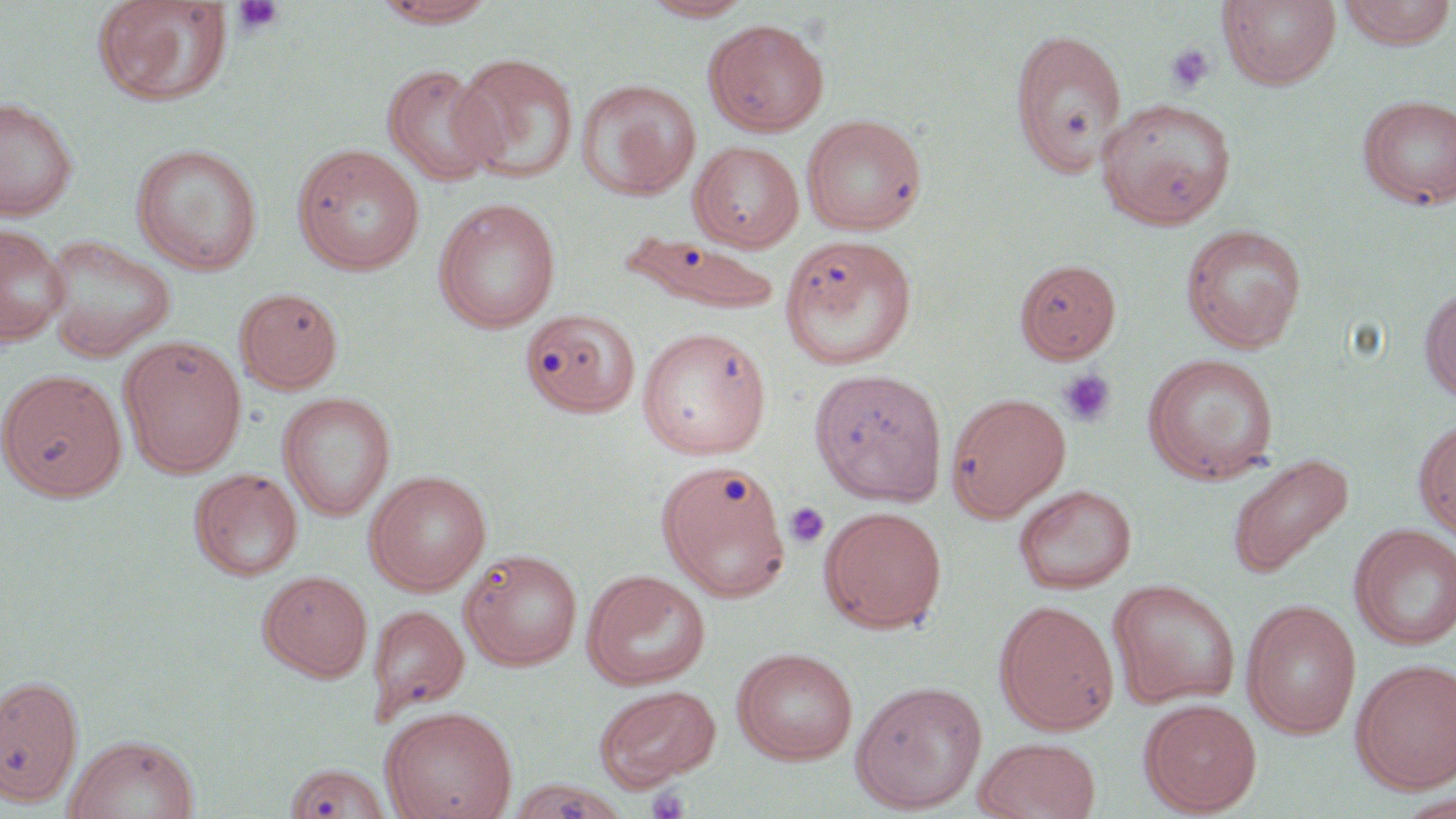
Approximate bounding boxes as named x1/y1/x2/y2 corners in pixels. Platelet locations: (x1=231, y1=0, x2=286, y2=36), (x1=1165, y1=43, x2=1215, y2=94), (x1=1058, y1=369, x2=1117, y2=427), (x1=784, y1=502, x2=830, y2=549), (x1=646, y1=787, x2=691, y2=819). Uninfected red blood cell locations: (x1=369, y1=0, x2=501, y2=27), (x1=640, y1=0, x2=755, y2=21), (x1=1218, y1=0, x2=1341, y2=90), (x1=1337, y1=0, x2=1455, y2=49), (x1=93, y1=1, x2=233, y2=107), (x1=703, y1=18, x2=830, y2=137), (x1=1009, y1=28, x2=1128, y2=177), (x1=449, y1=53, x2=581, y2=184), (x1=382, y1=64, x2=502, y2=187), (x1=577, y1=78, x2=700, y2=200), (x1=1357, y1=94, x2=1456, y2=210), (x1=0, y1=96, x2=79, y2=221), (x1=1096, y1=97, x2=1237, y2=230), (x1=801, y1=113, x2=928, y2=236), (x1=689, y1=141, x2=805, y2=252), (x1=131, y1=143, x2=262, y2=274), (x1=293, y1=144, x2=426, y2=275), (x1=433, y1=198, x2=562, y2=333), (x1=1180, y1=223, x2=1307, y2=353), (x1=0, y1=224, x2=70, y2=346), (x1=620, y1=233, x2=780, y2=313), (x1=42, y1=234, x2=176, y2=360), (x1=780, y1=234, x2=919, y2=371), (x1=1014, y1=258, x2=1121, y2=363), (x1=1419, y1=284, x2=1456, y2=404), (x1=234, y1=287, x2=344, y2=394), (x1=516, y1=308, x2=643, y2=419), (x1=636, y1=325, x2=772, y2=460), (x1=119, y1=335, x2=246, y2=476), (x1=1143, y1=353, x2=1279, y2=485), (x1=809, y1=368, x2=948, y2=506), (x1=1, y1=369, x2=127, y2=502), (x1=278, y1=392, x2=396, y2=521), (x1=946, y1=392, x2=1071, y2=521), (x1=1414, y1=417, x2=1456, y2=542), (x1=1225, y1=452, x2=1355, y2=580), (x1=657, y1=459, x2=791, y2=600), (x1=189, y1=468, x2=303, y2=581), (x1=365, y1=470, x2=491, y2=595), (x1=1014, y1=484, x2=1137, y2=595), (x1=820, y1=505, x2=947, y2=634), (x1=1349, y1=524, x2=1456, y2=651), (x1=460, y1=548, x2=583, y2=670), (x1=258, y1=570, x2=372, y2=682), (x1=582, y1=570, x2=711, y2=690), (x1=1107, y1=579, x2=1241, y2=710), (x1=1241, y1=599, x2=1361, y2=738), (x1=994, y1=600, x2=1120, y2=735), (x1=367, y1=604, x2=469, y2=720), (x1=732, y1=647, x2=859, y2=765), (x1=1352, y1=658, x2=1456, y2=794), (x1=0, y1=674, x2=84, y2=808), (x1=850, y1=680, x2=988, y2=814), (x1=594, y1=684, x2=721, y2=789), (x1=1139, y1=698, x2=1262, y2=816), (x1=380, y1=705, x2=519, y2=819), (x1=64, y1=733, x2=200, y2=819), (x1=973, y1=737, x2=1101, y2=819), (x1=283, y1=762, x2=392, y2=819). Slide-level diagnosis: no evidence of blood parasites. Image is 1456×819 pixels. Thin blood smear. Captured at 1000x magnification. Single field of view. Light microscopy. May-Grünwald-Giemsa-stained preparation.